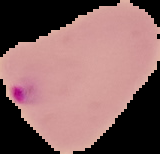
image size = 160×154 pixels
preparation = thin blood film
result = malaria parasites identified
image type = cell region segmented out of the field of view; surrounding area masked to black